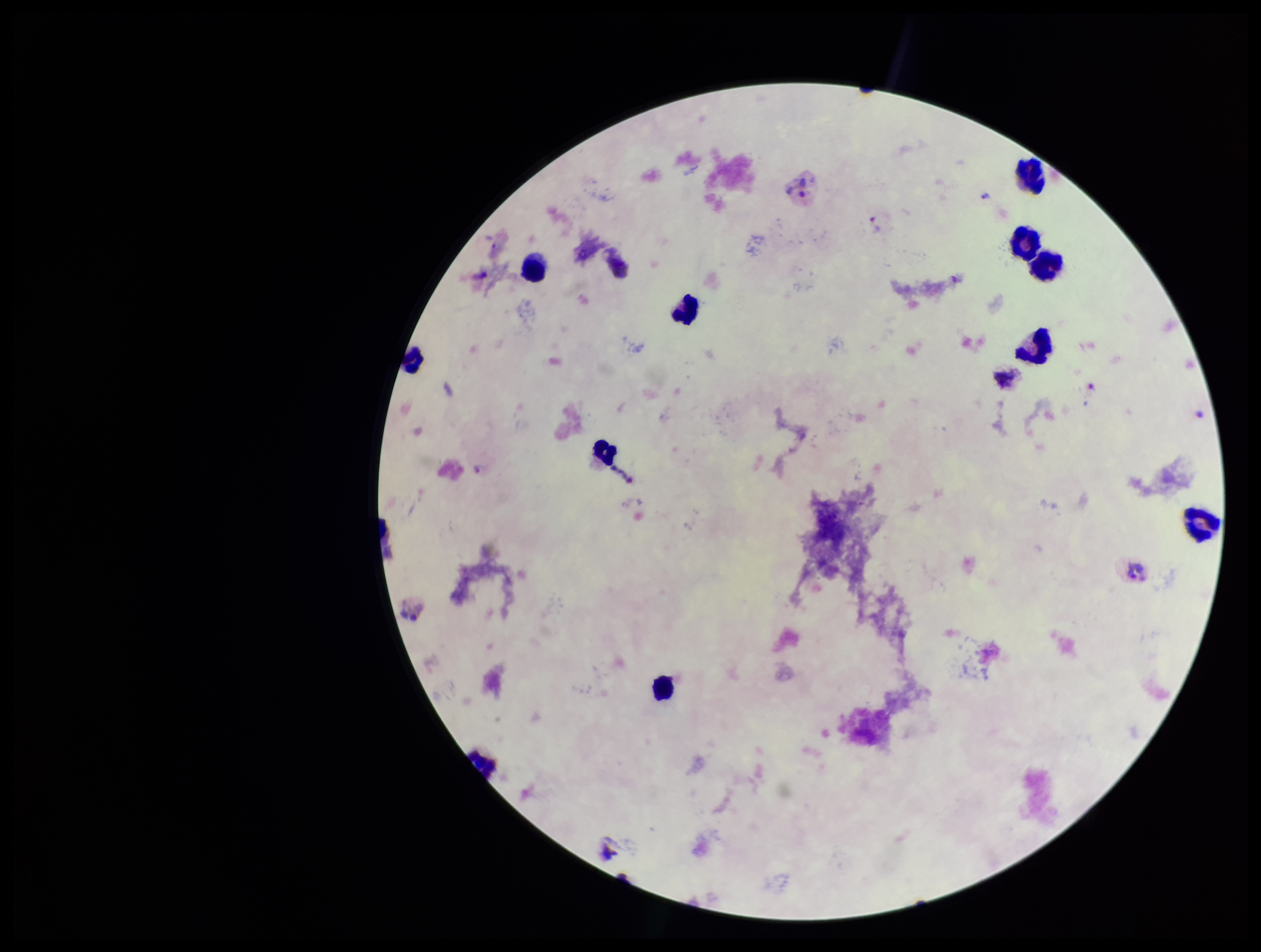

patient malaria status = positive
preparation = thick blood smear
image size = 1261×952 pixels
parasite count = 1
species reported for this patient = Plasmodium vivax
leukocyte count = 11
capture = smartphone photograph through the microscope eyepiece
Plasmodium parasites = seen
stain = Giemsa
field of view = single